Classify this cell by malaria status.
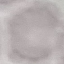
It is uninfected.

Thin blood smear. Giemsa-stained preparation. Cell patch, automatically extracted from a larger field of view and resized to 64 × 64 pixels. Photographed with a smartphone camera at the microscope eyepiece.